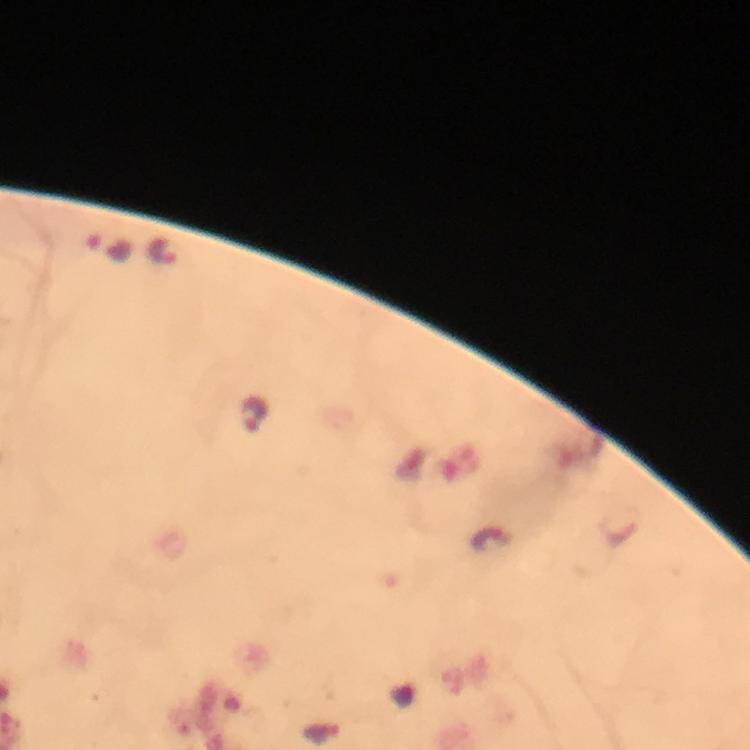

magnification = 100x
image size = 750×750 pixels
stain = Giemsa
context = from a malaria diagnostic workup
cropped from = a single field of view
immersion oil = applied
preparation = thick smear
Plasmodium parasite locations = approximate object centers, in pixels from the top-left corner: (x=108, y=246), (x=164, y=252), (x=255, y=413)
capture = smartphone mounted on the microscope